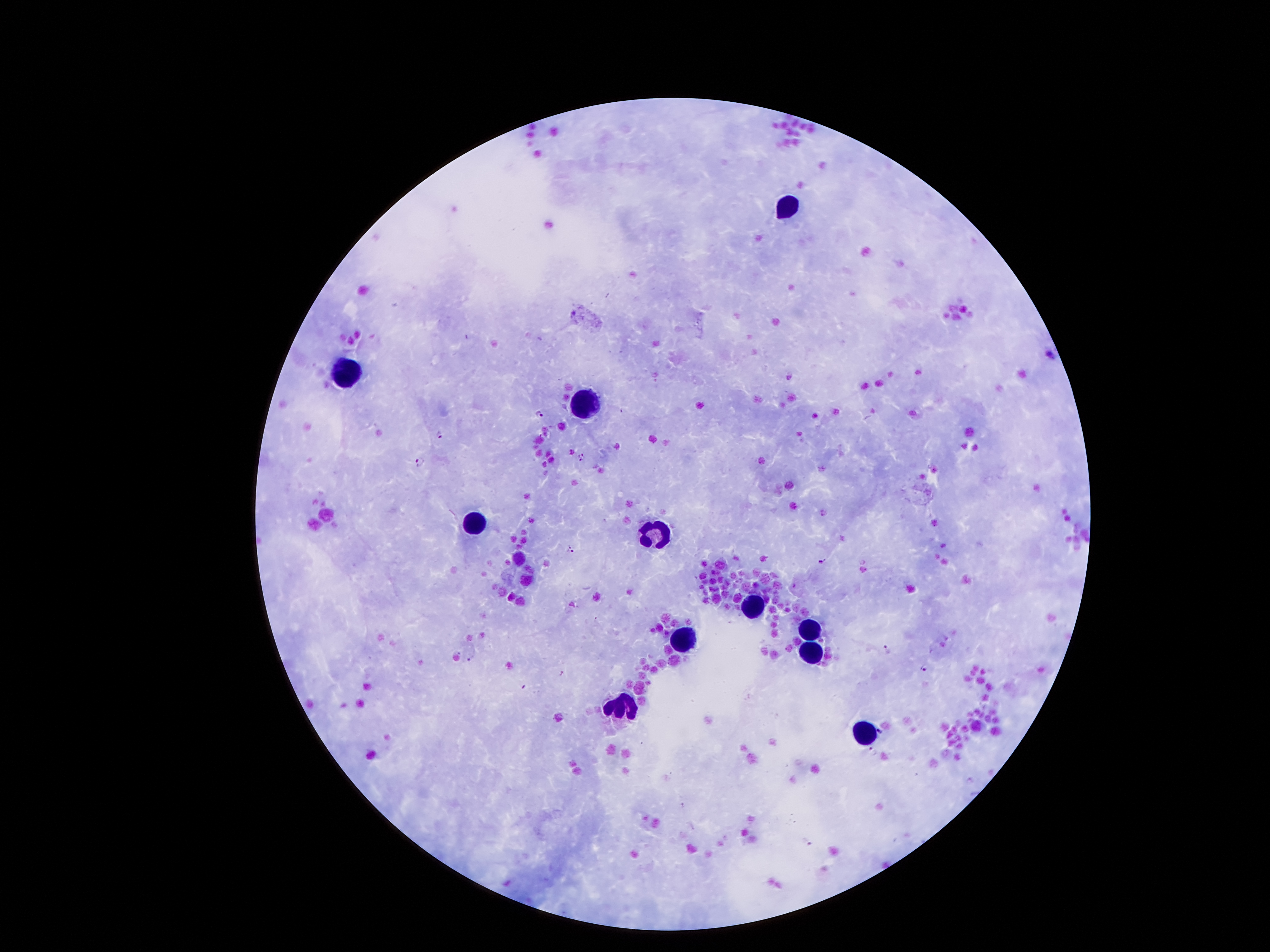

Giemsa stain. Thick peripheral-blood smear. Smartphone photograph taken through the microscope eyepiece. Patient malaria status: positive for Plasmodium falciparum. 100x magnification. Image is 1270×952 pixels. One field from this slide.